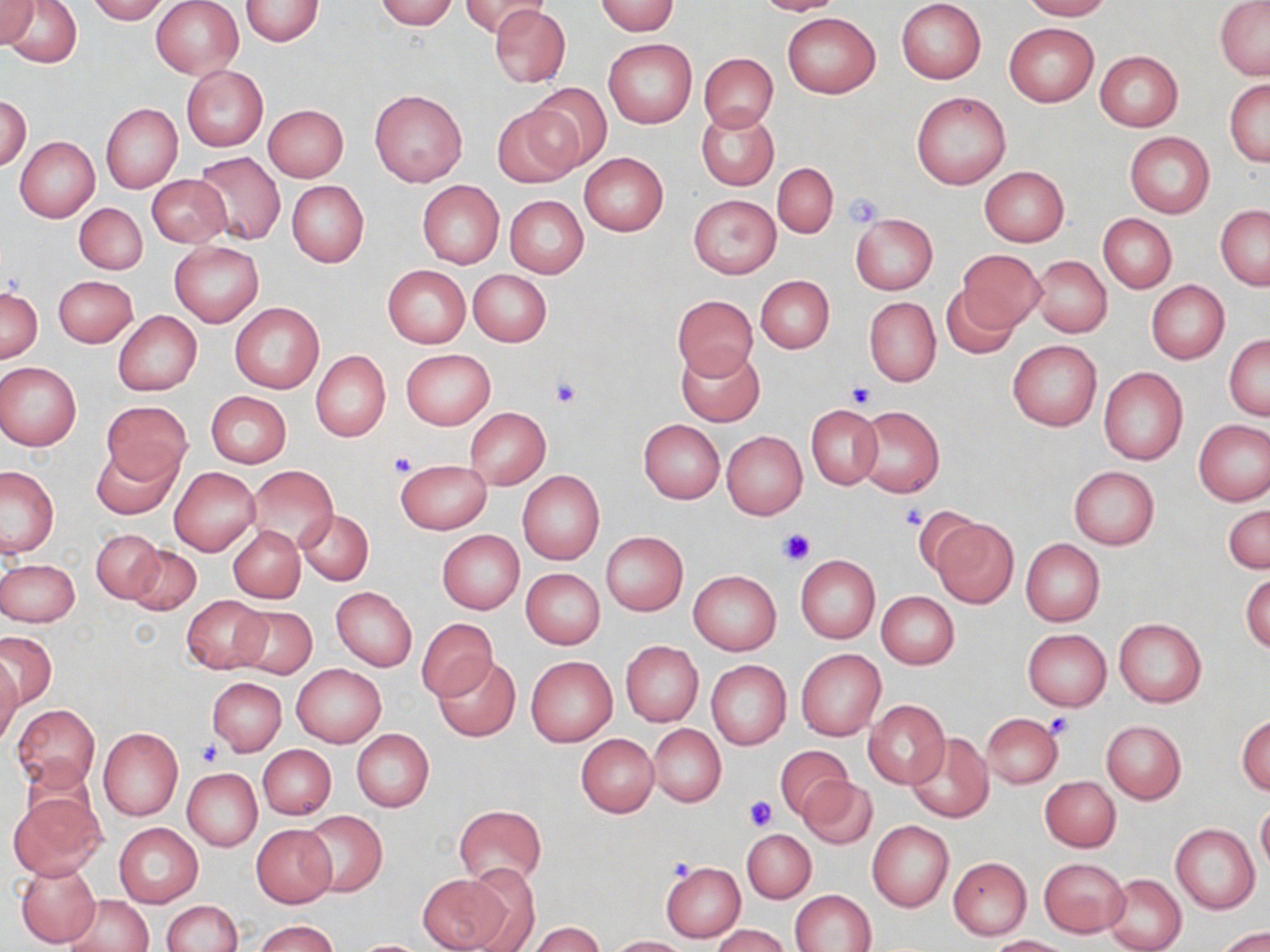
slide-level diagnosis = no evidence of blood parasites
magnification = 1000x
image size = 1270×952 pixels
modality = optical microscopy
stain = May-Grünwald-Giemsa
platelet locations = approximate bounding boxes as (x1, y1, x2, y2) in pixels: (842, 193, 885, 228), (551, 376, 581, 408), (846, 380, 875, 409), (387, 451, 417, 477), (898, 506, 926, 530), (775, 527, 816, 563), (1045, 712, 1074, 740), (197, 741, 220, 766), (743, 794, 776, 830), (666, 857, 699, 884)
preparation = thin blood film
field of view = one of a larger specimen
uninfected red blood cell locations = approximate bounding boxes as (x1, y1, x2, y2) in pixels: (0, 0, 39, 47), (4, 0, 81, 67), (87, 0, 170, 24), (151, 0, 243, 78), (240, 0, 323, 46), (373, 0, 458, 30), (458, 0, 549, 37), (752, 0, 846, 15), (896, 0, 986, 84), (1020, 0, 1113, 20), (1216, 0, 1270, 79), (593, 1, 680, 35), (489, 4, 570, 88), (781, 12, 880, 98), (1004, 22, 1098, 105), (603, 38, 697, 129), (1094, 50, 1183, 131), (698, 53, 777, 132), (181, 65, 268, 151), (1225, 79, 1270, 166), (525, 84, 610, 174), (368, 88, 468, 187), (911, 91, 1011, 189), (1, 97, 31, 170), (101, 103, 182, 193), (264, 104, 349, 182), (493, 106, 582, 188), (696, 107, 779, 190), (1125, 133, 1215, 217), (15, 137, 99, 221), (194, 152, 285, 245), (579, 153, 668, 235), (773, 162, 838, 239), (979, 166, 1069, 247), (147, 175, 231, 248), (286, 180, 369, 266), (417, 180, 504, 267), (688, 194, 781, 279), (504, 195, 588, 278), (74, 202, 147, 275), (1216, 205, 1270, 290), (851, 214, 937, 294), (1098, 214, 1176, 292), (170, 241, 264, 326), (957, 249, 1044, 330), (1030, 256, 1112, 338), (382, 265, 471, 348), (468, 269, 552, 347), (54, 275, 138, 347), (754, 275, 834, 353), (1146, 281, 1229, 363), (940, 284, 1021, 359), (0, 287, 41, 362), (672, 294, 758, 377), (863, 296, 940, 386), (230, 302, 325, 393), (112, 310, 201, 396), (1225, 335, 1270, 420), (1007, 340, 1102, 431), (675, 344, 764, 425), (401, 348, 494, 430), (311, 351, 390, 442), (0, 362, 81, 450), (1098, 367, 1187, 465), (198, 390, 281, 534), (207, 393, 291, 468), (100, 402, 191, 486), (806, 404, 882, 488), (852, 405, 945, 498), (465, 406, 550, 490), (638, 419, 725, 503), (1194, 420, 1270, 505), (722, 431, 807, 518), (89, 441, 180, 520), (396, 459, 490, 534), (1, 466, 58, 557), (169, 466, 259, 556), (246, 466, 337, 550), (1069, 466, 1159, 548), (517, 470, 604, 566), (1223, 503, 1269, 574), (295, 508, 374, 585), (930, 517, 1019, 607), (229, 525, 304, 602), (93, 529, 163, 604), (437, 530, 523, 615), (601, 532, 688, 615), (1020, 538, 1105, 626), (126, 545, 201, 616), (795, 555, 879, 643), (2, 559, 79, 627), (521, 568, 604, 649), (689, 570, 782, 655), (1241, 570, 1269, 654), (331, 587, 417, 670), (876, 591, 959, 669), (181, 596, 269, 672), (230, 604, 317, 677), (416, 617, 497, 701), (1113, 618, 1207, 707), (1023, 628, 1111, 710), (0, 630, 56, 710), (621, 641, 702, 726), (796, 649, 886, 740), (432, 654, 519, 741), (525, 655, 617, 746), (0, 656, 21, 747), (706, 659, 791, 750), (291, 663, 386, 747), (207, 677, 286, 756), (864, 700, 949, 787), (12, 704, 99, 789), (981, 713, 1063, 789), (1236, 713, 1270, 795), (1101, 721, 1186, 803), (648, 724, 726, 806), (97, 727, 182, 821), (351, 729, 433, 812), (576, 733, 659, 817), (906, 733, 994, 822), (258, 745, 336, 820), (775, 745, 851, 821), (183, 769, 263, 851), (1041, 776, 1120, 852), (799, 777, 877, 850), (9, 793, 104, 878), (1256, 802, 1270, 875), (453, 804, 546, 887), (300, 811, 388, 897), (866, 820, 953, 912), (114, 822, 203, 907), (1170, 823, 1259, 913), (251, 824, 338, 907), (742, 828, 816, 902), (947, 856, 1031, 940), (1039, 857, 1127, 936), (16, 861, 101, 948), (660, 861, 745, 941), (461, 865, 540, 950), (417, 873, 512, 952), (1102, 874, 1186, 952), (789, 889, 877, 952), (64, 895, 152, 952), (161, 900, 241, 952), (252, 919, 341, 952), (528, 922, 605, 952), (711, 925, 789, 952), (1216, 928, 1269, 952), (610, 935, 688, 951), (988, 935, 1069, 951), (354, 940, 425, 952)